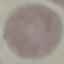
Result: no malaria parasites detected. Giemsa stain. Photographed with a smartphone camera at the microscope eyepiece. Thin blood film. Automatically extracted cell patch, resized to 64 × 64 pixels.